Assess the morphology of the red blood cells.
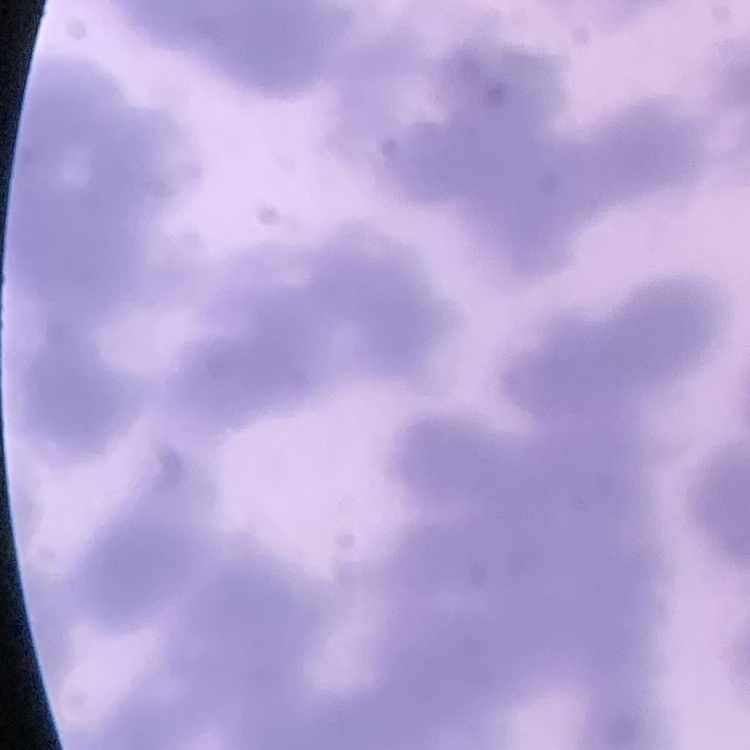
They show rouleaux formation.

{
  "stain": "Field's or Giemsa",
  "image_type": "one tile cut from a larger photomicrograph",
  "preparation": "thin peripheral smear"
}